Assess the morphology of the erythrocytes.
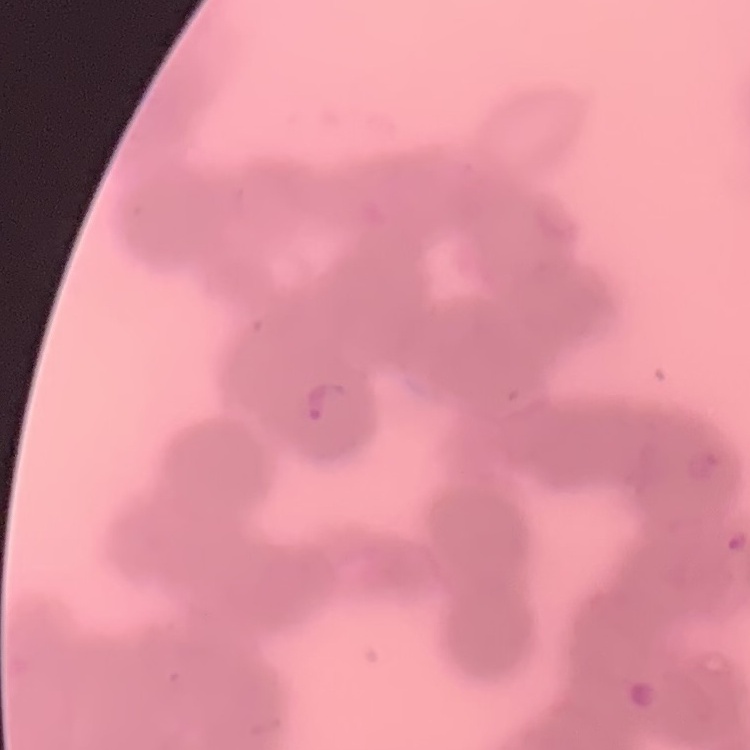
Rouleaux formation.

Stained with either Field's or Giemsa. Square crop of a larger photomicrograph. Thin blood film.